Classify this cell by malaria status.
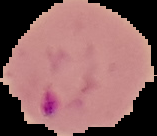
Parasitized.

image type = segmented cell region with the area outside set to black
image size = 157×136 pixels
preparation = thin blood film